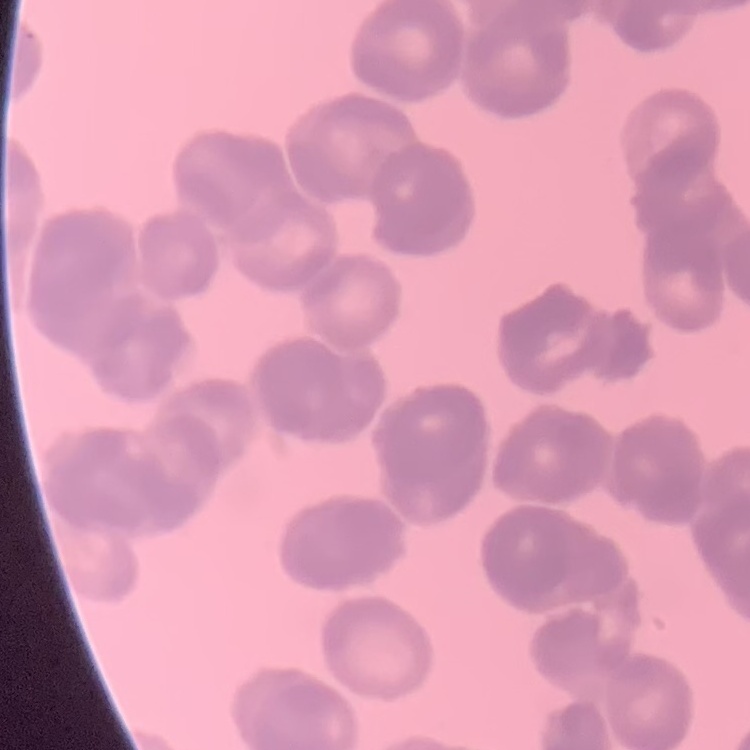

The erythrocytes show rouleaux formation. Thin blood smear. Stained with either Field's or Giemsa. Square crop of a larger photomicrograph.